Locate every Plasmodium ovale-infected red blood cell.
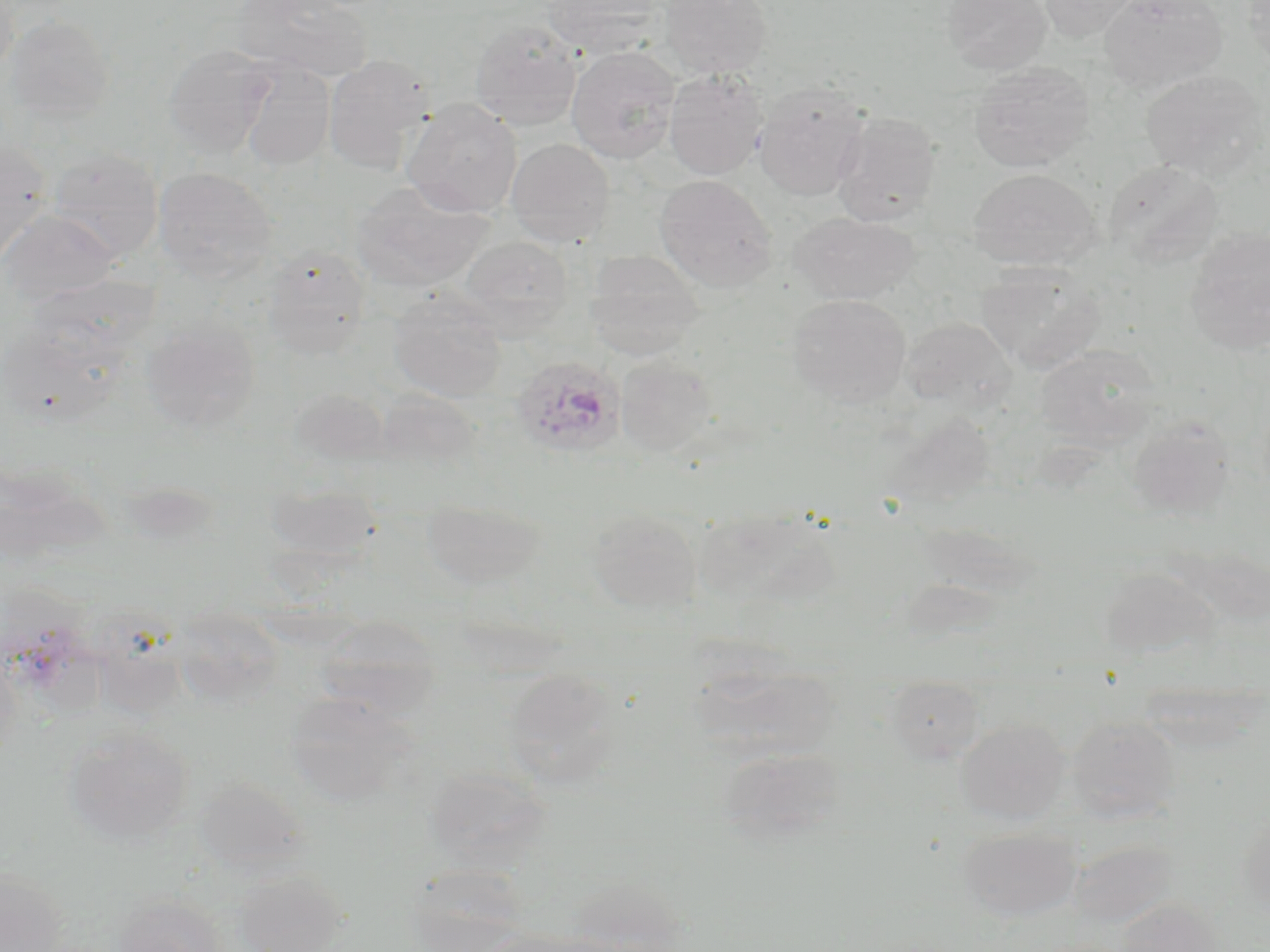
Approximate bounding boxes as [x1, y1, x2, y2] in pixels.
Plasmodium ovale-infected red blood cells: [510, 355, 626, 458].

Summary:
  - Uninfected red blood cell locations: [0, 0, 19, 80], [232, 0, 374, 80], [543, 0, 667, 58], [659, 0, 772, 79], [941, 0, 1052, 75], [1037, 0, 1140, 42], [1098, 0, 1228, 93], [1242, 0, 1270, 73], [4, 15, 114, 125], [469, 20, 583, 130], [163, 43, 276, 157], [565, 46, 681, 163], [322, 55, 433, 173], [238, 60, 336, 170], [968, 62, 1095, 172], [1140, 69, 1269, 181], [663, 70, 768, 181], [753, 81, 870, 201], [402, 97, 523, 217], [831, 111, 943, 226], [506, 138, 615, 248], [0, 142, 51, 265], [47, 147, 164, 261], [1103, 159, 1225, 269], [154, 167, 277, 284], [968, 168, 1100, 271], [653, 174, 778, 292], [350, 181, 493, 294], [1, 211, 120, 307], [789, 211, 918, 305], [1185, 225, 1270, 356], [457, 235, 574, 337], [262, 246, 372, 358], [584, 250, 704, 359], [976, 262, 1106, 373], [387, 289, 507, 402], [787, 294, 911, 408], [900, 316, 1017, 412], [141, 319, 261, 434], [1036, 344, 1162, 449], [615, 357, 717, 456], [290, 389, 392, 466], [370, 389, 483, 474], [1127, 414, 1235, 520], [0, 461, 90, 566], [265, 479, 381, 562], [421, 497, 547, 589], [699, 506, 843, 608], [586, 507, 703, 612], [1098, 566, 1221, 662], [316, 616, 441, 717], [93, 632, 189, 722], [0, 647, 21, 769], [691, 660, 839, 762], [503, 669, 624, 789], [885, 675, 985, 765], [284, 692, 416, 807], [1067, 715, 1181, 822], [955, 718, 1070, 824], [63, 726, 195, 846], [718, 747, 848, 845], [424, 765, 551, 873], [193, 776, 307, 874], [958, 827, 1081, 923], [1068, 839, 1179, 928], [407, 866, 530, 950], [0, 868, 68, 951], [233, 869, 349, 951], [569, 877, 686, 949], [113, 894, 228, 952], [1115, 899, 1223, 951]
  - Slide-level diagnosis: Plasmodium ovale
  - Modality: optical microscopy
  - Field of view: one of a larger specimen
  - Preparation: thin blood smear
  - Magnification: 1000x
  - Image size: 1270×952 pixels
  - Stain: May-Grünwald-Giemsa